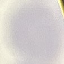

Result: negative for malaria parasites. Photographed with a smartphone camera at the microscope eyepiece. Automatically extracted cell patch, resized to 64 × 64 pixels. Thin blood smear. Giemsa stain.